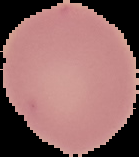

image size = 139×157 pixels
preparation = thin blood film
image type = cell region segmented out of the field of view; surrounding area masked to black
malaria status = uninfected